Outline each uninfected red blood cell.
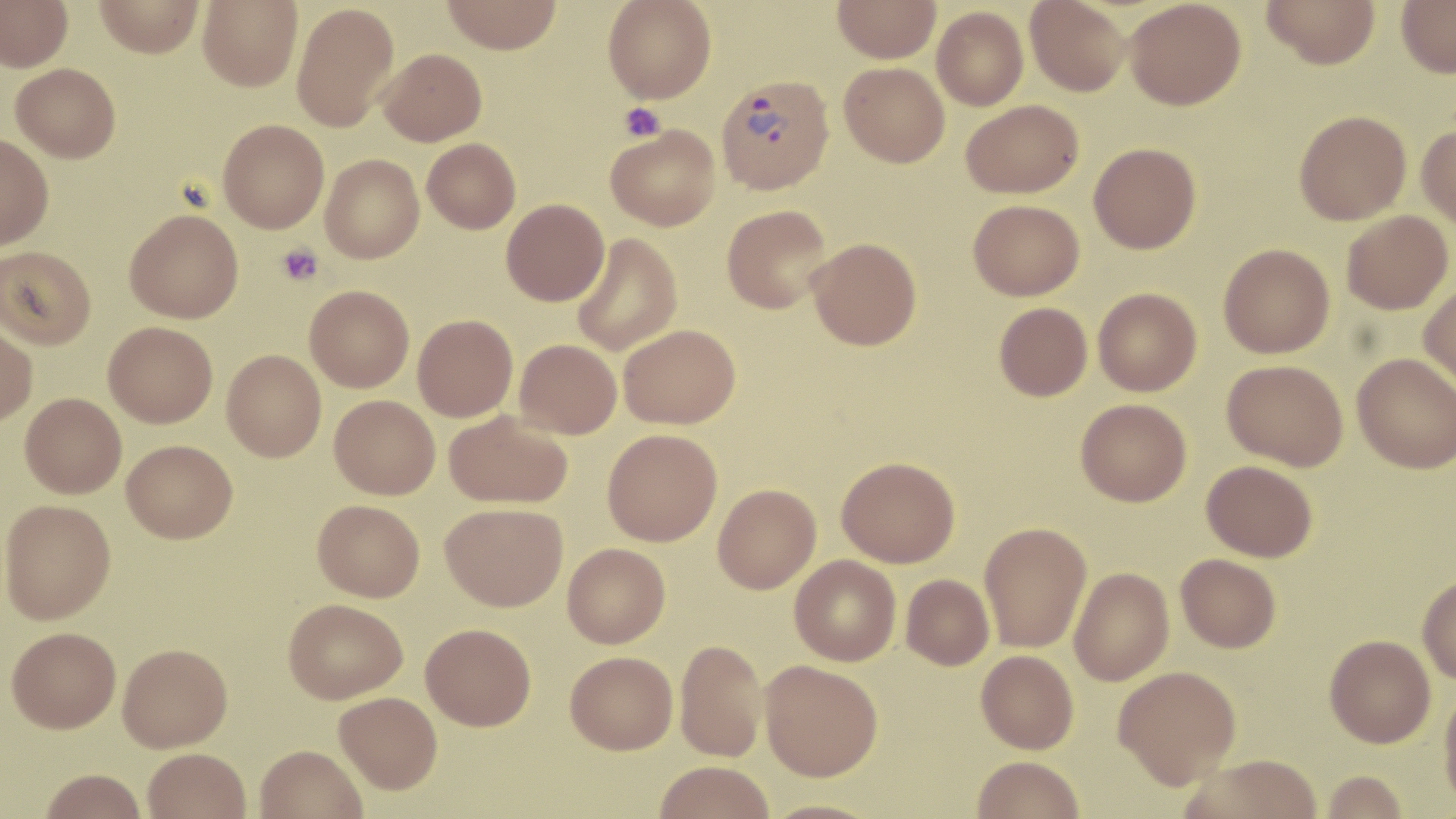

Approximate bounding boxes as [x1, y1, x2, y2] in pixels.
Uninfected red blood cells: [0, 0, 73, 71], [94, 0, 204, 57], [198, 0, 302, 91], [442, 0, 563, 54], [603, 0, 716, 103], [833, 0, 941, 63], [1025, 0, 1131, 97], [1124, 0, 1246, 110], [1261, 0, 1380, 69], [1396, 0, 1456, 78], [292, 2, 399, 133], [931, 7, 1029, 110], [378, 48, 487, 146], [11, 62, 121, 162], [839, 62, 950, 168], [961, 99, 1084, 198], [1294, 110, 1411, 225], [218, 119, 329, 233], [605, 124, 721, 231], [1416, 124, 1456, 228], [0, 134, 54, 249], [422, 138, 521, 233], [1089, 142, 1201, 254], [320, 154, 424, 263], [501, 199, 609, 305], [968, 199, 1084, 300], [722, 204, 833, 314], [125, 209, 243, 323], [1341, 210, 1453, 314], [571, 233, 682, 357], [807, 237, 922, 350], [1218, 243, 1335, 358], [1, 246, 96, 349], [1418, 282, 1456, 394], [305, 285, 414, 392], [1093, 287, 1202, 396], [994, 302, 1093, 401], [413, 315, 518, 422], [0, 321, 38, 425], [103, 321, 217, 427], [619, 324, 740, 429], [514, 339, 622, 439], [222, 349, 326, 461], [1352, 352, 1456, 473], [1222, 359, 1348, 471], [20, 393, 127, 498], [330, 395, 440, 499], [1076, 398, 1192, 506], [444, 410, 573, 509], [602, 429, 722, 546], [121, 439, 237, 542], [836, 456, 960, 567], [1202, 460, 1318, 561], [713, 483, 821, 593], [0, 499, 116, 624], [313, 499, 425, 601], [440, 502, 567, 611], [979, 522, 1091, 652], [562, 543, 670, 648], [1176, 554, 1281, 652], [789, 555, 901, 666], [1069, 567, 1174, 685], [901, 574, 994, 669], [1417, 574, 1456, 684], [283, 598, 408, 703], [421, 623, 536, 730], [6, 626, 121, 732], [1324, 634, 1435, 747], [675, 639, 767, 761], [118, 642, 232, 751], [976, 650, 1078, 754], [565, 651, 678, 754], [760, 660, 883, 781], [1113, 665, 1241, 789], [1438, 685, 1456, 811], [334, 691, 442, 793], [255, 744, 368, 819], [143, 748, 251, 819], [1182, 754, 1323, 818], [972, 756, 1085, 818], [653, 760, 775, 819], [39, 768, 147, 818], [1321, 770, 1408, 818], [761, 799, 884, 819].

{
  "slide_level_diagnosis": "Plasmodium vivax",
  "field_of_view": "one of a larger specimen",
  "platelet_locations": "approximate bounding boxes as [x1, y1, x2, y2] in pixels: [618, 103, 666, 142], [276, 243, 324, 286]",
  "modality": "optical microscopy",
  "plasmodium_vivax_infected_red_blood_cell_locations": "approximate bounding boxes as [x1, y1, x2, y2] in pixels: [716, 73, 835, 194]",
  "magnification": "1000x",
  "stain": "May-Grünwald-Giemsa",
  "image_size": "1456×819 pixels",
  "preparation": "thin blood film"
}